Assess this cell for malaria.
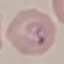
Parasitized.

Automatically extracted cell patch, resized to 64 × 64 pixels. Giemsa-stained preparation. Photographed with a smartphone camera at the microscope eyepiece. Thin smear of blood.